Locate every uninfected red blood cell.
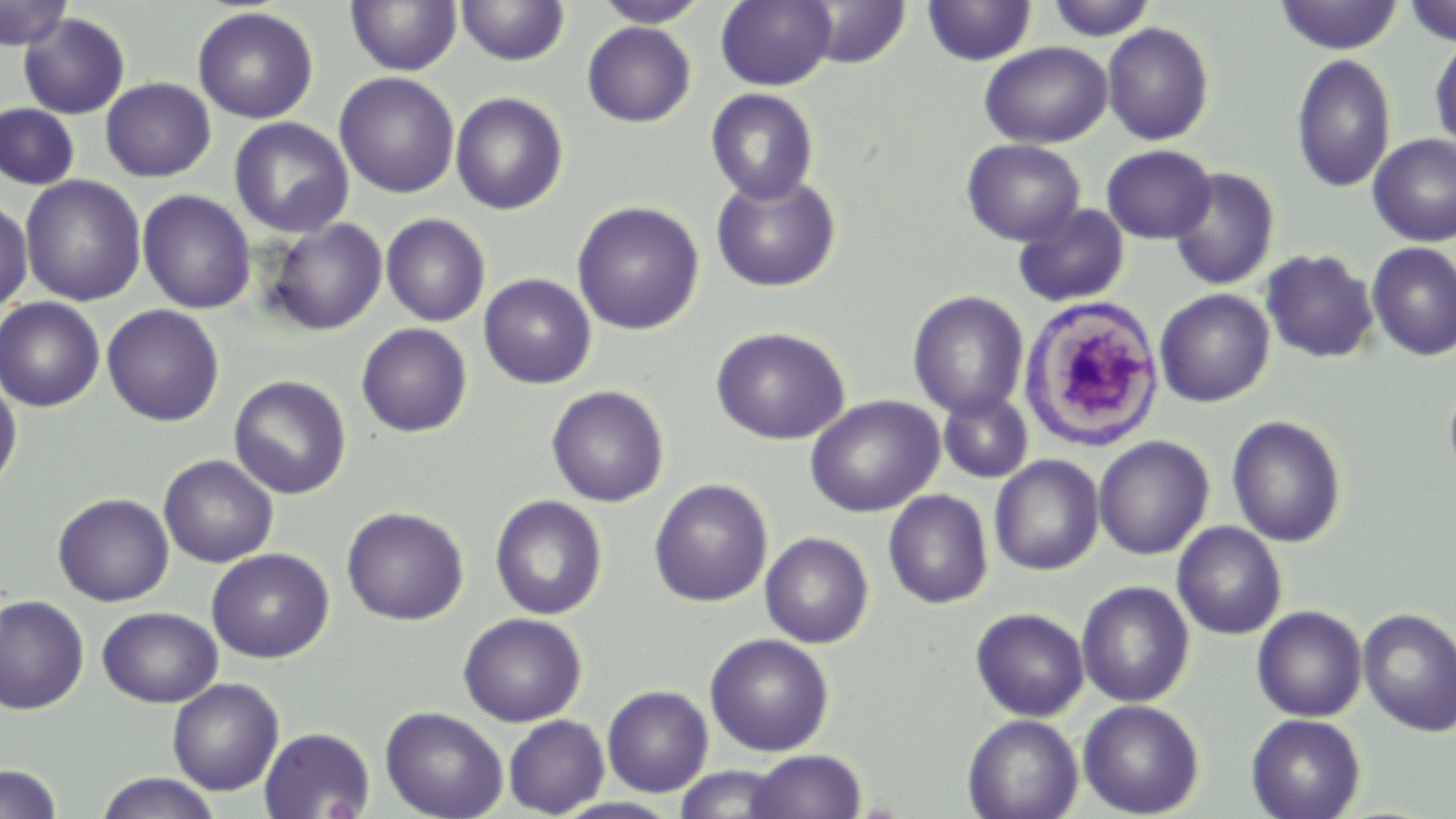
Approximate bounding boxes as named x1/y1/x2/y2 corners in pixels.
Uninfected red blood cells: (x1=0, y1=0, x2=73, y2=50), (x1=346, y1=0, x2=462, y2=76), (x1=456, y1=0, x2=570, y2=67), (x1=593, y1=0, x2=711, y2=27), (x1=716, y1=0, x2=836, y2=90), (x1=922, y1=0, x2=1036, y2=66), (x1=1045, y1=0, x2=1157, y2=41), (x1=1401, y1=0, x2=1456, y2=47), (x1=803, y1=1, x2=911, y2=69), (x1=1274, y1=1, x2=1403, y2=54), (x1=192, y1=6, x2=319, y2=124), (x1=18, y1=13, x2=130, y2=119), (x1=582, y1=22, x2=696, y2=127), (x1=1101, y1=22, x2=1215, y2=146), (x1=1430, y1=36, x2=1456, y2=154), (x1=979, y1=42, x2=1112, y2=149), (x1=1291, y1=53, x2=1396, y2=193), (x1=335, y1=72, x2=459, y2=198), (x1=101, y1=77, x2=215, y2=182), (x1=706, y1=88, x2=818, y2=204), (x1=451, y1=92, x2=568, y2=215), (x1=1, y1=103, x2=79, y2=190), (x1=229, y1=117, x2=354, y2=238), (x1=1368, y1=134, x2=1456, y2=247), (x1=962, y1=139, x2=1085, y2=246), (x1=1101, y1=145, x2=1216, y2=243), (x1=1169, y1=167, x2=1280, y2=291), (x1=710, y1=173, x2=842, y2=292), (x1=21, y1=175, x2=146, y2=306), (x1=137, y1=190, x2=256, y2=314), (x1=0, y1=199, x2=33, y2=313), (x1=572, y1=202, x2=705, y2=335), (x1=1013, y1=203, x2=1130, y2=308), (x1=381, y1=214, x2=490, y2=326), (x1=263, y1=218, x2=388, y2=335), (x1=1366, y1=242, x2=1456, y2=361), (x1=1261, y1=249, x2=1378, y2=363), (x1=479, y1=274, x2=597, y2=389), (x1=1154, y1=288, x2=1275, y2=407), (x1=908, y1=290, x2=1029, y2=419), (x1=0, y1=297, x2=105, y2=411), (x1=102, y1=305, x2=224, y2=426), (x1=357, y1=323, x2=472, y2=437), (x1=711, y1=327, x2=850, y2=445), (x1=229, y1=375, x2=351, y2=499), (x1=0, y1=378, x2=22, y2=495), (x1=1443, y1=380, x2=1456, y2=484), (x1=546, y1=385, x2=669, y2=507), (x1=939, y1=390, x2=1033, y2=483), (x1=804, y1=395, x2=945, y2=517), (x1=1227, y1=415, x2=1346, y2=547), (x1=1093, y1=435, x2=1214, y2=560), (x1=159, y1=454, x2=278, y2=567), (x1=989, y1=454, x2=1104, y2=576), (x1=649, y1=479, x2=773, y2=606), (x1=883, y1=489, x2=993, y2=608), (x1=53, y1=493, x2=174, y2=606), (x1=490, y1=495, x2=607, y2=620), (x1=342, y1=506, x2=468, y2=625), (x1=1172, y1=522, x2=1286, y2=640), (x1=760, y1=532, x2=873, y2=648), (x1=206, y1=548, x2=334, y2=663), (x1=1076, y1=581, x2=1195, y2=708), (x1=0, y1=594, x2=89, y2=714), (x1=1252, y1=605, x2=1367, y2=722), (x1=97, y1=606, x2=223, y2=708), (x1=970, y1=607, x2=1089, y2=722), (x1=1358, y1=607, x2=1456, y2=737), (x1=458, y1=612, x2=587, y2=727), (x1=705, y1=633, x2=834, y2=756), (x1=168, y1=678, x2=284, y2=795), (x1=602, y1=685, x2=714, y2=797), (x1=1078, y1=699, x2=1204, y2=818), (x1=503, y1=703, x2=713, y2=807), (x1=380, y1=706, x2=508, y2=819), (x1=962, y1=714, x2=1083, y2=819), (x1=1246, y1=714, x2=1365, y2=819), (x1=504, y1=715, x2=609, y2=817), (x1=259, y1=727, x2=375, y2=819), (x1=745, y1=749, x2=866, y2=819), (x1=0, y1=764, x2=63, y2=819), (x1=674, y1=765, x2=791, y2=819), (x1=95, y1=772, x2=221, y2=819).

White blood cell locations: (x1=1019, y1=294, x2=1164, y2=451). Slide-level diagnosis: negative for blood parasites. Single field of view. Image is 1456×819 pixels. Thin blood smear. 1000x magnification. May-Grünwald-Giemsa stain. Optical microscopy.